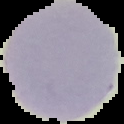
Result: no malaria parasites seen. The area outside the segmented cell region is set to black. From a thin blood film. Image is 124×124 pixels.